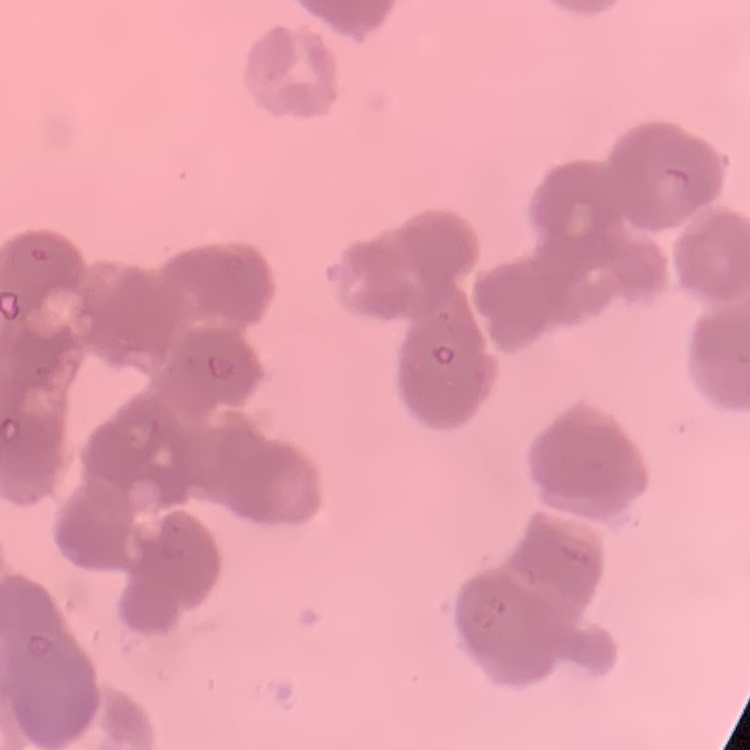

Summary:
  - Erythrocyte morphology: rouleaux formation
  - Stain: Field's or Giemsa
  - Image type: square crop of a larger photomicrograph
  - Preparation: thin blood smear